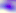

Toxoplasma gondii is shown. Captured at 400x magnification. Micrograph.